Assess this cell for malaria.
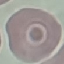

Uninfected.

Summary:
  - Stain: Giemsa
  - Image type: cell patch, automatically extracted from a larger field of view and resized to 64 × 64 pixels
  - Capture: smartphone through the microscope eyepiece
  - Preparation: thin blood smear